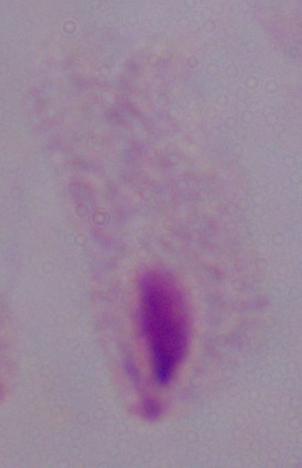

Photomicrograph. 1000x magnification. A trichomonad is seen.